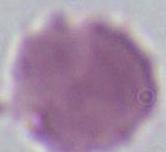
Summary:
  - Magnification: 1000x
  - Identification: red blood cell
  - Modality: micrograph